Look for Plasmodium parasites.
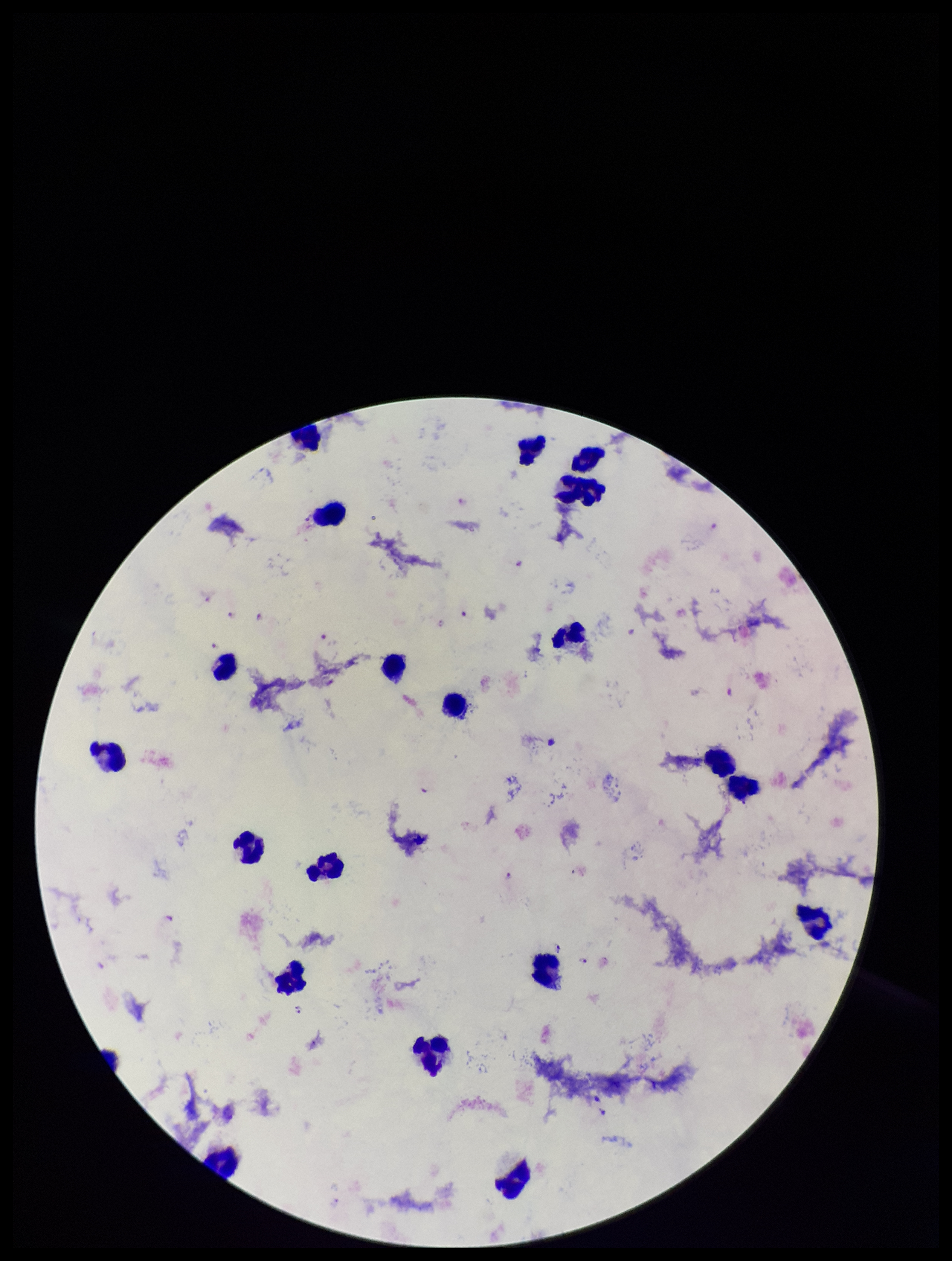

Identified.

Single field of view. Species reported for this patient: Plasmodium falciparum. Giemsa stain. Leukocyte count: 20. Parasite count: 11. Smartphone photograph taken through the eyepiece of a microscope. Patient malaria status: infected. Image is 952×1261 pixels. Preparation: thick blood smear.